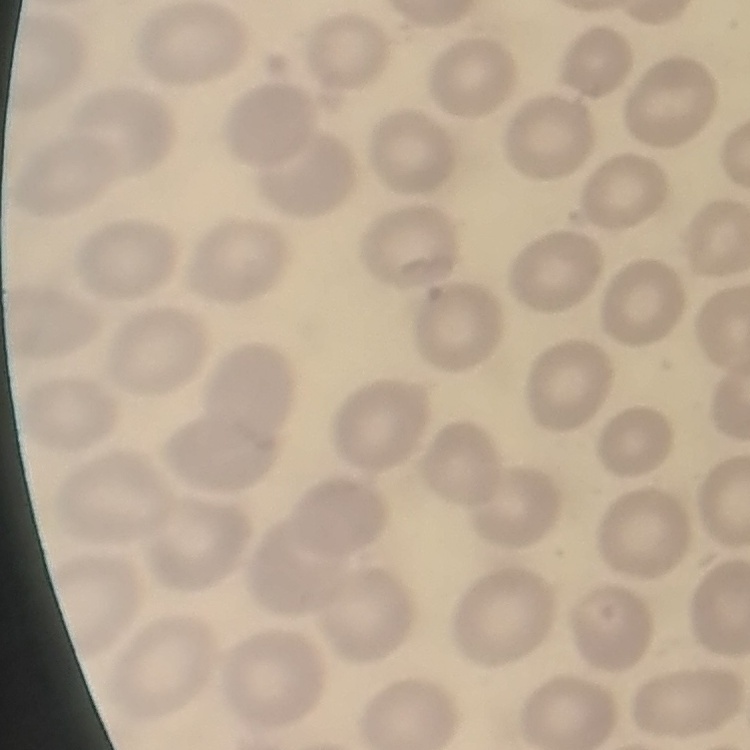
Summary:
  - Red blood cell morphology: no rouleaux formation
  - Image type: one tile cut from a larger photomicrograph
  - Preparation: thin peripheral smear
  - Stain: Field's or Giemsa